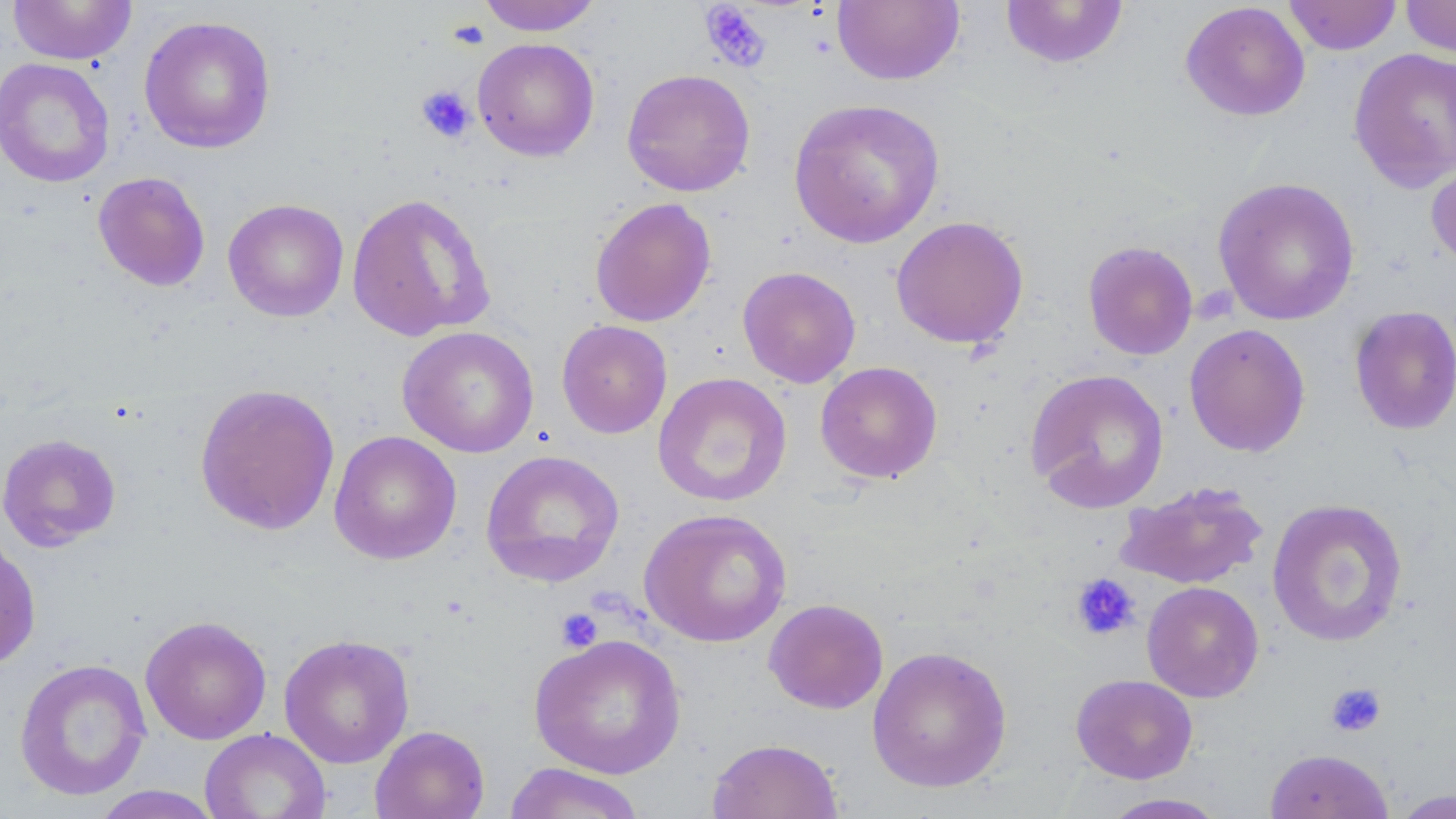

Approximate bounding boxes as (x1, y1, x2, y2) in pixels. Platelet locations: (698, 2, 772, 72), (449, 18, 489, 50), (416, 85, 476, 143), (1071, 573, 1141, 642), (555, 607, 603, 652), (1325, 682, 1386, 737). Uninfected red blood cell locations: (7, 0, 136, 65), (476, 0, 603, 35), (832, 0, 964, 86), (1284, 0, 1402, 55), (1400, 0, 1456, 59), (1000, 1, 1129, 69), (1180, 2, 1310, 122), (138, 15, 276, 154), (472, 37, 600, 162), (1348, 47, 1456, 193), (0, 58, 115, 187), (622, 68, 756, 197), (788, 98, 946, 249), (1426, 155, 1456, 271), (92, 171, 211, 292), (1212, 176, 1360, 326), (345, 193, 495, 342), (589, 197, 716, 327), (223, 198, 349, 322), (890, 215, 1029, 349), (1082, 241, 1198, 360), (737, 266, 861, 388), (1349, 305, 1456, 435), (556, 319, 672, 439), (1184, 323, 1311, 457), (397, 326, 540, 458), (815, 361, 943, 484), (1025, 368, 1169, 513), (652, 371, 792, 508), (194, 383, 340, 536), (329, 430, 462, 565), (0, 433, 121, 551), (481, 450, 625, 588), (1113, 480, 1269, 590), (1267, 498, 1408, 647), (638, 507, 793, 647), (0, 534, 41, 671), (1141, 581, 1264, 703), (763, 598, 889, 714), (140, 615, 272, 745), (278, 633, 415, 769), (528, 633, 687, 779), (867, 645, 1013, 793), (14, 658, 152, 801), (1070, 673, 1198, 784), (369, 725, 490, 819), (199, 728, 331, 819), (706, 738, 844, 819), (1264, 748, 1394, 819), (502, 762, 648, 818), (89, 785, 225, 818), (1389, 789, 1455, 818), (1101, 793, 1228, 818). Slide-level diagnosis: negative for blood parasites. One field of a larger specimen. Optical microscopy. May-Grünwald-Giemsa stain. Captured at 1000x magnification. Thin blood film. Image is 1456×819 pixels.